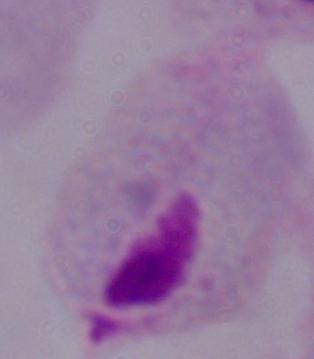
Summary:
  - Magnification: 1000x
  - Modality: micrograph
  - Identification: trichomonad